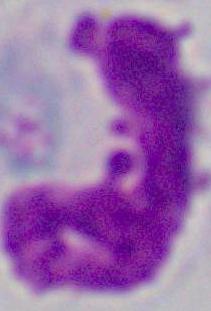 Captured at 1000x magnification. A leukocyte is seen. Photomicrograph.